Describe the morphology of the erythrocytes.
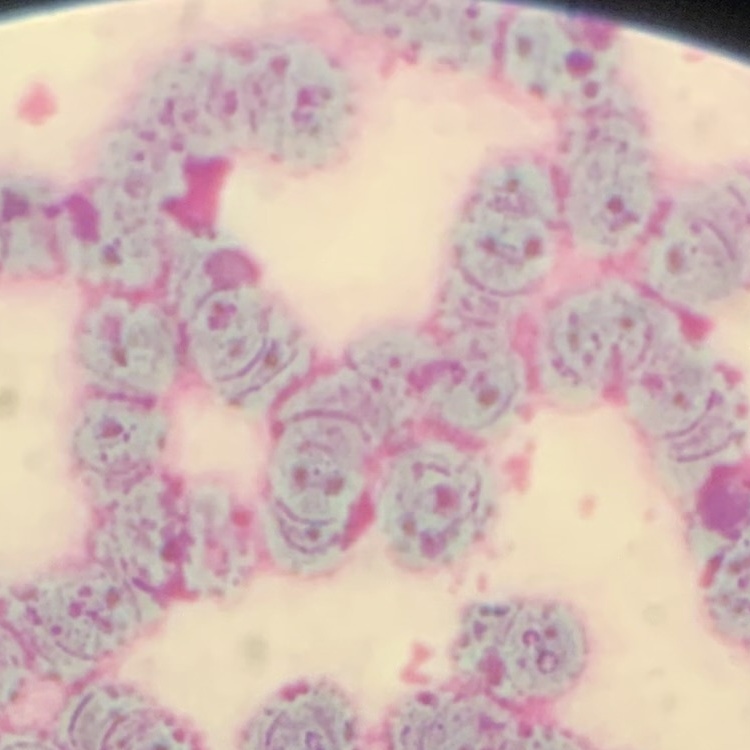
Rouleaux formation.

stain = Field's or Giemsa
preparation = thin blood smear
image type = square crop of a larger photomicrograph